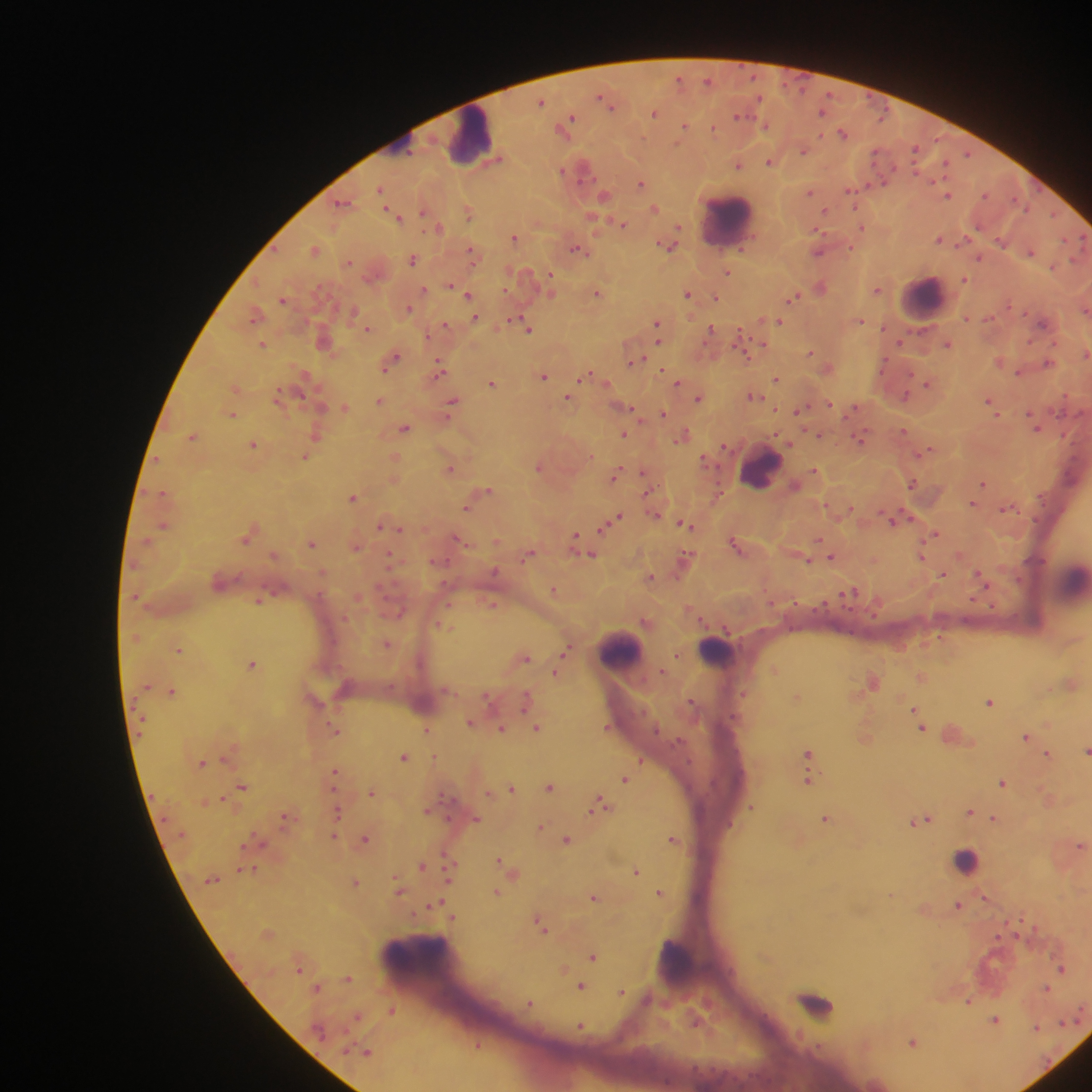
capture = mobile-phone photograph through a microscope
image size = 1092×1092 pixels
country = Ghana
malaria parasite locations = approximate centers as x y in pixels: 707 81; 541 101; 607 101; 824 110; 655 112; 566 123; 685 125; 766 125; 714 127; 843 133; 917 149; 803 150; 770 162; 738 163; 947 163; 583 168; 641 183; 380 190; 852 190; 810 191; 948 195; 604 196; 344 203; 655 208; 825 211; 424 212; 469 212; 397 216; 623 224; 438 227; 861 227; 515 237; 940 239; 1001 241; 668 244; 314 250; 578 250; 818 250; 473 252; 1031 252; 979 257; 413 259; 349 262; 728 272; 965 278; 549 280; 452 286; 821 286; 878 289; 424 291; 598 293; 688 293; 468 294; 795 297; 716 298; 284 299; 409 308; 1086 310; 256 314; 967 317; 474 318; 860 320; 779 321; 1046 322; 445 326; 527 326; 367 328; 658 328; 710 332; 324 341; 262 344; 762 344; 948 344; 811 352; 1086 353; 392 359; 635 361; 1001 361; 1048 363; 829 367; 440 368; 663 370; 1020 371; 543 375; 586 377; 776 378; 678 382; 492 383; 928 383; 236 388; 753 395; 906 395; 280 396; 700 397; 569 398; 380 401; 828 403; 991 403; 452 404; 344 407; 627 408; 801 410; 233 414; 663 414; 1036 426; 405 427; 903 432; 317 433; 624 435; 683 435; 820 435; 193 436; 861 436; 254 443; 925 451; 304 456; 396 457; 705 460; 540 466; 450 468; 815 470; 644 473; 615 474; 913 483; 984 484; 487 490; 354 496; 973 504; 468 507; 1007 508; 655 514; 617 518; 896 518; 611 523; 686 524; 163 525; 381 526; 398 528; 936 533; 249 535; 459 540; 576 540; 819 541; 312 542; 736 543; 356 546; 583 550; 528 554; 591 554; 832 556; 921 556; 389 557; 685 558; 809 560; 943 574; 651 576; 980 576; 554 589; 848 593; 259 600; 492 604; 646 622; 446 626; 388 643; 179 649; 566 649; 678 655; 525 657; 253 663; 775 669; 663 670; 555 673; 922 677; 874 681; 1072 683; 172 691; 488 696; 798 696; 526 701; 990 701; 916 711; 471 722; 608 726; 922 726; 537 727; 334 728; 503 728; 428 729; 865 736; 1026 736; 1086 751; 808 753; 1049 754; 405 756; 641 760; 202 762; 335 773; 626 778; 808 779; 1003 782; 550 786; 243 787; 512 788; 372 791; 489 793; 222 798; 600 804; 752 807; 428 810; 970 811; 338 812; 285 816; 476 818; 826 818; 994 818; 922 819; 541 827; 335 835; 365 838; 673 838; 568 839; 1081 845; 447 856; 499 860; 421 865; 247 869; 514 870; 636 871; 449 877; 356 882; 399 890; 497 891; 660 892; 891 895; 595 896; 985 897; 441 903; 435 904; 958 904; 452 917; 541 923; 593 955; 563 969; 1062 969; 349 978; 583 986; 318 987; 1047 987; 622 992; 969 1001; 530 1003; 392 1010; 358 1015; 996 1019; 1061 1021; 581 1026; 1036 1028; 913 1041; 478 1044; 366 1051
preparation = thick blood film
leukocyte locations = approximate centers as x y in pixels: 472 136; 728 220; 925 298; 761 468; 1071 582; 621 652; 716 652; 965 861; 424 960; 675 962; 816 1004
field of view = single